Outline every leukocyte.
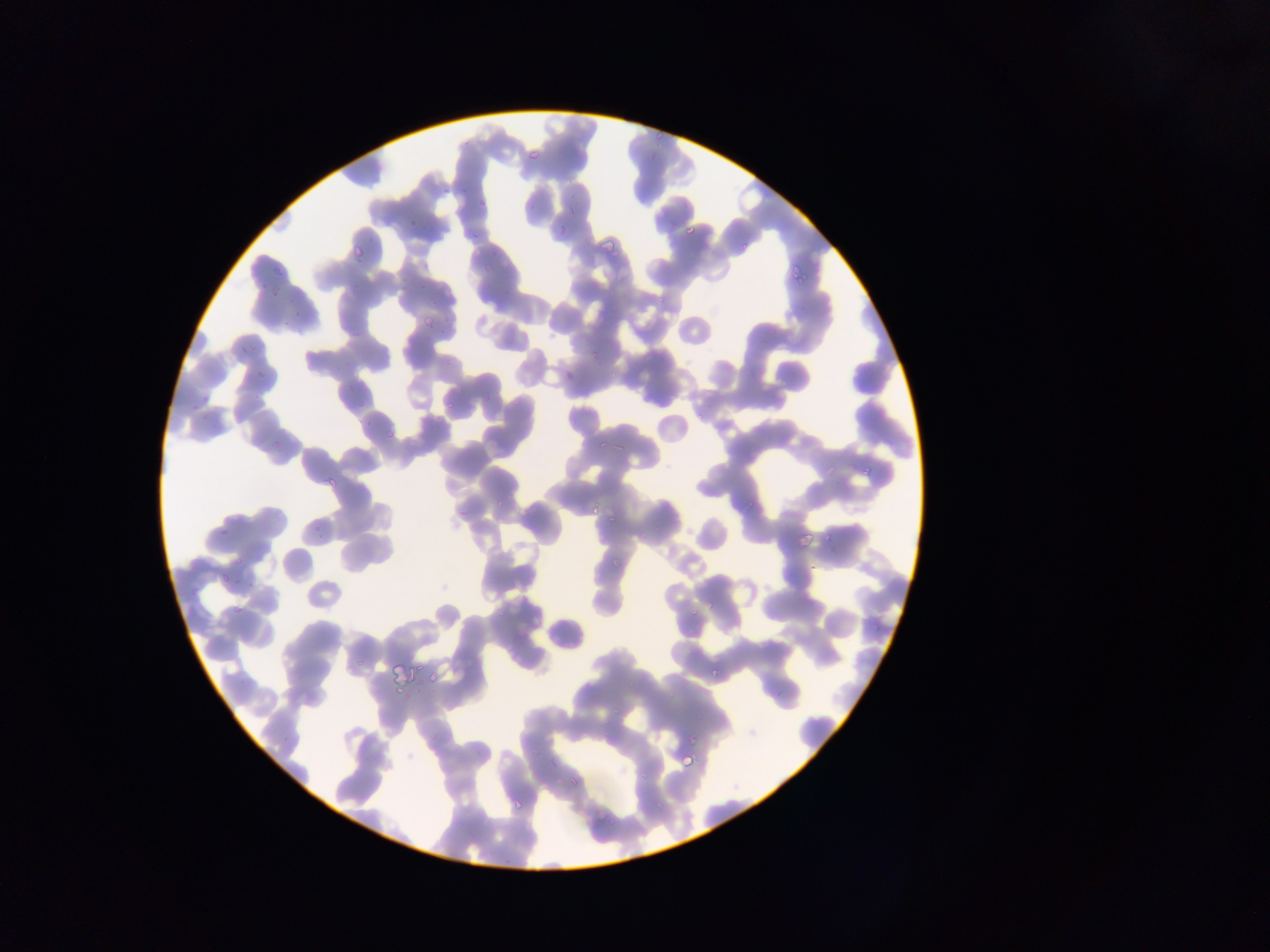
No leukocytes observed.

Approximate bounding boxes as left top right bottom in pixels. Malaria parasite locations: 652 128 663 140; 526 149 540 162; 648 151 660 164; 440 186 451 196; 478 200 486 208; 564 205 576 217; 407 218 418 228; 681 220 700 239; 557 225 564 238; 593 229 620 257; 350 241 365 259; 271 260 285 271; 792 260 813 282; 258 281 268 291; 267 291 281 301; 288 309 301 320; 419 310 438 330; 232 340 251 360; 256 369 270 384; 563 370 575 382; 202 396 212 406; 446 400 457 412; 188 405 194 416; 384 428 394 439; 612 442 624 454; 861 461 873 475; 323 473 340 491; 587 505 604 515; 604 509 618 523; 606 515 617 526; 311 519 325 539; 215 523 229 537; 797 528 813 544; 824 528 836 545; 612 556 622 568; 228 557 245 568; 805 560 822 578; 218 573 230 586; 701 596 715 610; 231 600 247 617; 354 650 372 666; 707 663 723 678; 423 671 437 685; 394 682 404 697; 612 706 621 717; 671 720 703 753; 680 753 696 769; 568 774 581 788; 512 797 524 811; 501 855 513 864. Photographed through a microscope with a mobile-phone camera. Thin blood film. Collected in Ghana. Image is 1270×952 pixels. One field of view.